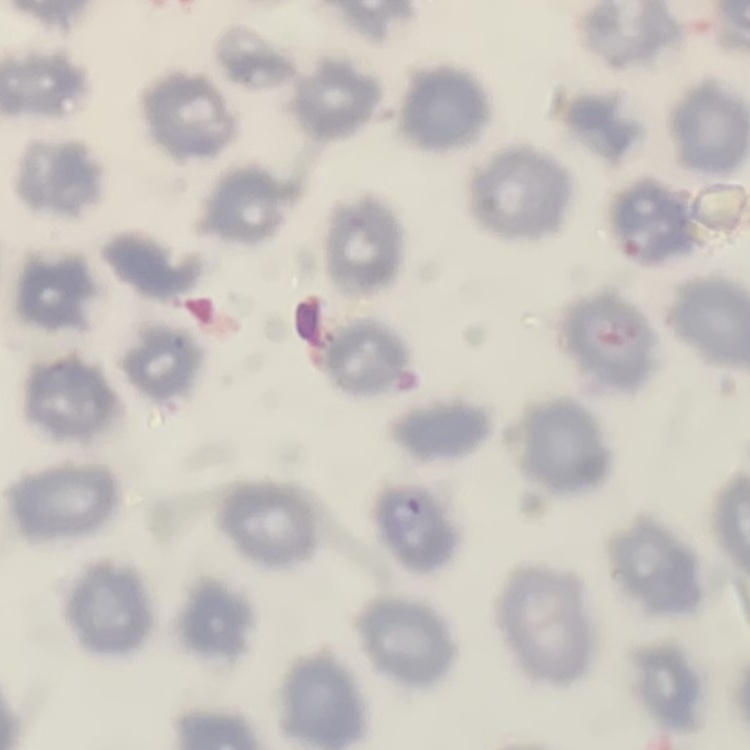
Summary:
  - Red blood cell morphology: no rouleaux formation
  - Preparation: thin blood film
  - Image type: square crop of a larger photomicrograph
  - Stain: Field's or Giemsa